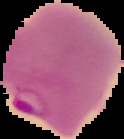
Summary:
  - Image type: segmented cell region with the area outside set to black
  - Image size: 124×139 pixels
  - Preparation: thin blood smear
  - Result: Plasmodium parasites detected